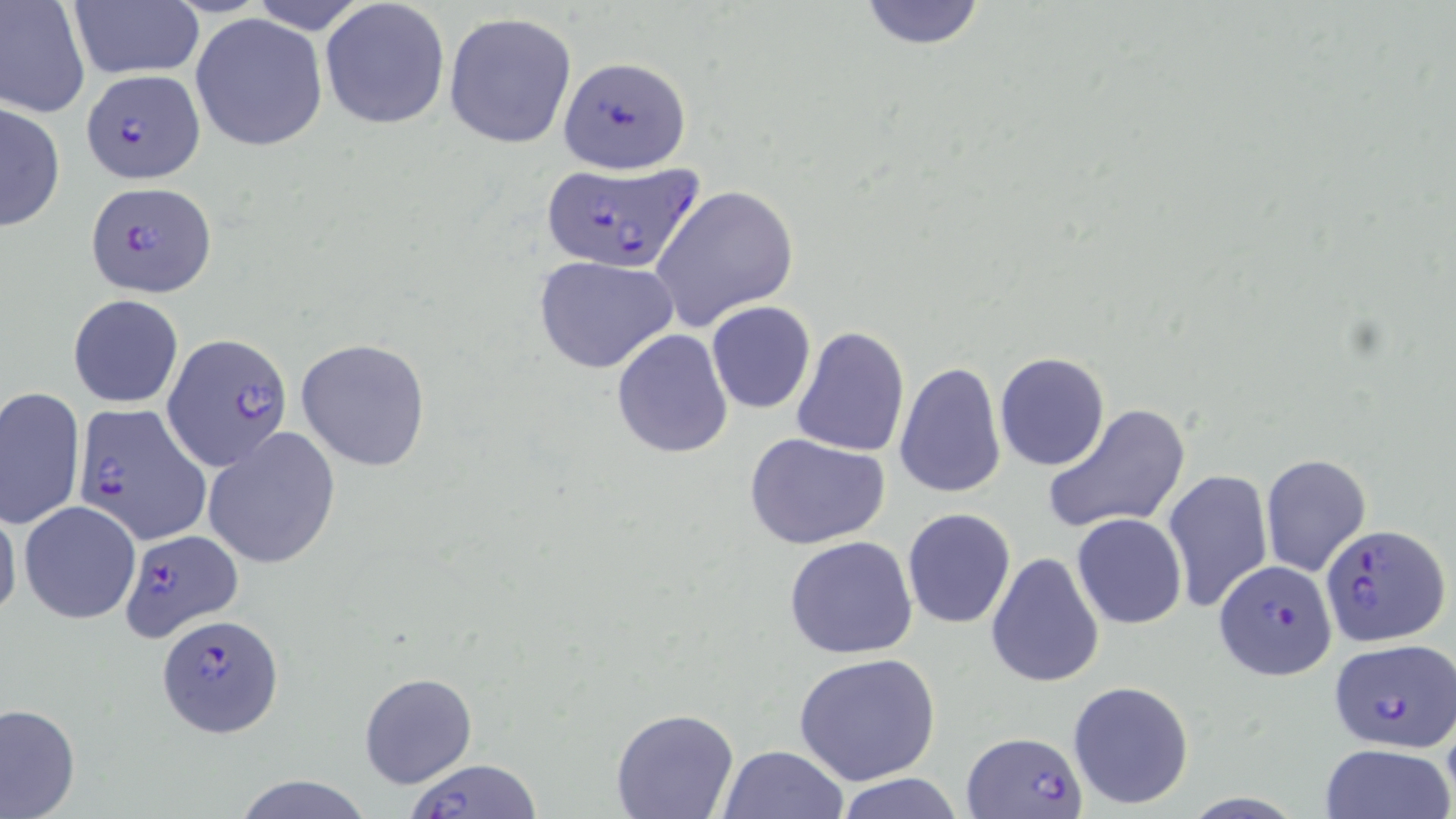

slide-level diagnosis = Plasmodium falciparum
uninfected red blood cell locations = approximate bounding boxes as (x1,y1)-(x2,y2) corner pairs in pixels: (69,0)-(204,80), (247,0)-(371,33), (320,0)-(451,130), (857,0)-(989,52), (0,1)-(91,119), (443,11)-(576,148), (190,13)-(329,153), (0,100)-(66,234), (650,185)-(800,331), (533,254)-(679,375), (68,294)-(184,409), (705,301)-(816,415), (789,325)-(910,456), (611,329)-(735,459), (295,337)-(432,472), (994,351)-(1111,472), (894,360)-(1007,499), (0,386)-(85,530), (1042,403)-(1189,536), (203,427)-(340,568), (746,431)-(891,550), (1259,453)-(1372,577), (1162,468)-(1274,613), (18,500)-(143,624), (0,504)-(22,627), (902,509)-(1015,628), (1071,513)-(1188,630), (784,535)-(918,660), (985,551)-(1106,689), (794,653)-(939,787), (359,672)-(478,790), (1066,679)-(1195,811), (0,701)-(80,819), (610,708)-(739,819), (1317,744)-(1454,819), (717,745)-(849,819), (234,774)-(374,819), (836,774)-(963,818)
modality = optical microscopy
stain = May-Grünwald-Giemsa
magnification = 1000x
field of view = one of a larger specimen
Plasmodium falciparum-infected red blood cell locations = approximate bounding boxes as (x1,y1)-(x2,y2) corner pairs in pixels: (558,56)-(692,175), (80,71)-(204,183), (540,162)-(702,274), (85,179)-(216,297), (163,332)-(294,470), (75,403)-(211,546), (1320,523)-(1450,650), (117,528)-(243,643), (1214,559)-(1338,680), (157,613)-(283,738), (1330,640)-(1454,751), (961,731)-(1088,819), (402,756)-(545,819)
image size = 1456×819 pixels
preparation = thin blood film